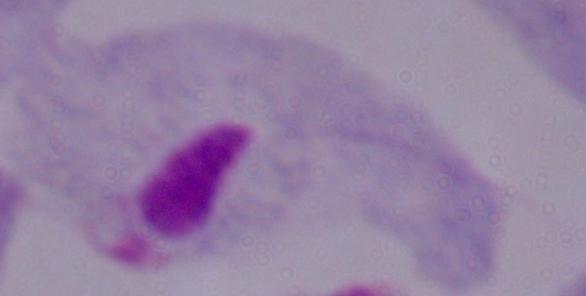

Summary:
  - Magnification: 1000x
  - Identification: trichomonad
  - Modality: photomicrograph